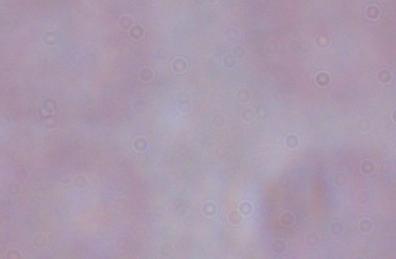

{
  "identification": "trypanosome",
  "modality": "photomicrograph",
  "magnification": "1000x"
}